State which parasite is depicted.
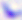
This is Toxoplasma gondii.

Summary:
  - Magnification: 400x
  - Modality: photomicrograph